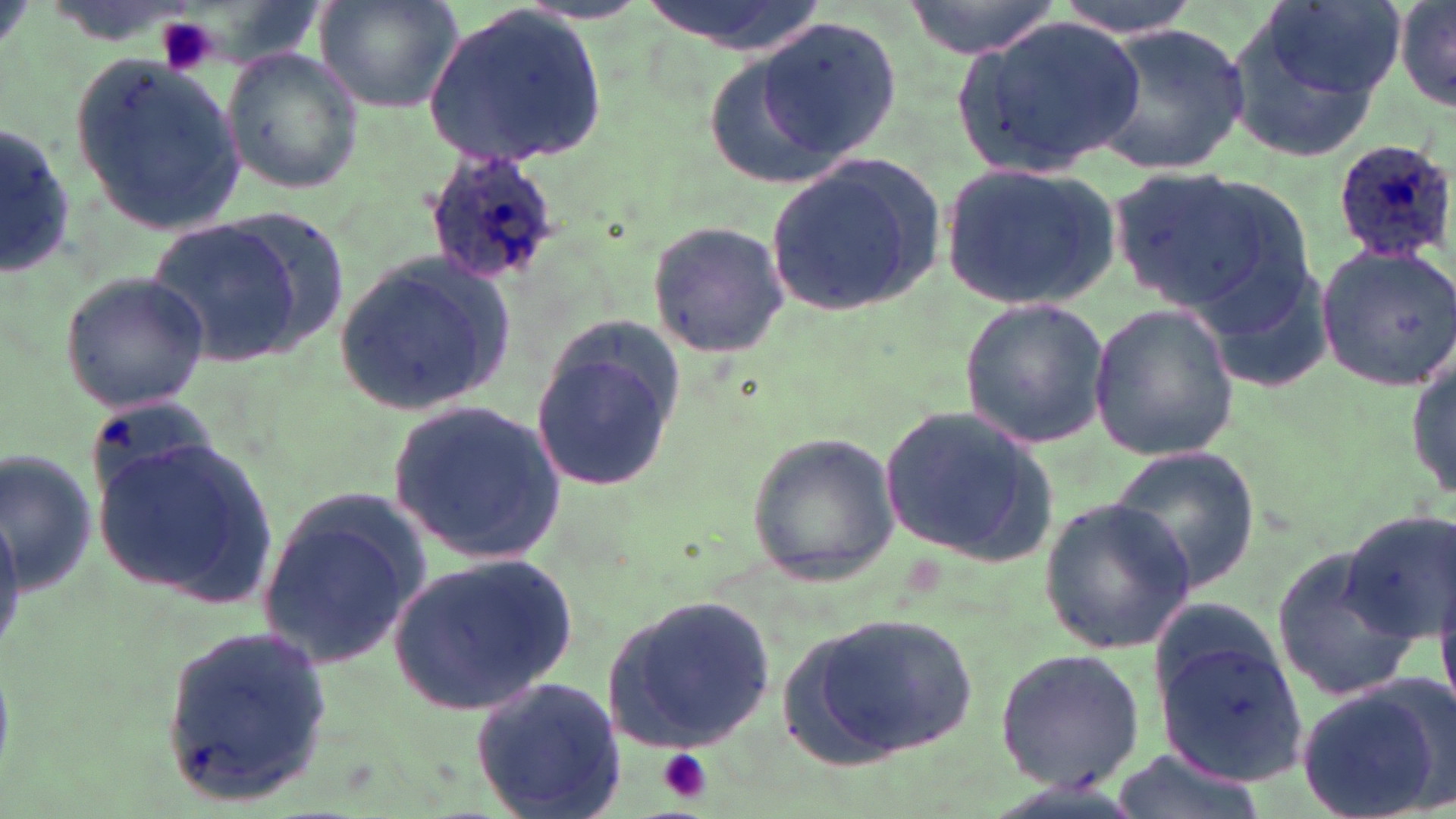
Summary:
  - Coordinate format: approximate bounding boxes as [x1, y1, x2, y2] in pixels
  - Uninfected red blood cell locations: [315, 0, 464, 115], [636, 0, 825, 55], [899, 0, 1070, 60], [1049, 0, 1201, 37], [1224, 0, 1404, 159], [1393, 0, 1455, 113], [424, 3, 605, 168], [954, 14, 1144, 180], [750, 16, 901, 169], [1087, 20, 1252, 177], [223, 47, 366, 196], [70, 50, 245, 235], [0, 127, 77, 278], [765, 152, 947, 319], [936, 161, 1121, 311], [1107, 163, 1311, 325], [149, 216, 306, 366], [644, 218, 792, 361], [1315, 242, 1456, 394], [333, 251, 518, 417], [58, 272, 210, 414], [957, 296, 1110, 450], [1086, 302, 1241, 462], [528, 318, 687, 496], [1408, 347, 1454, 504], [386, 397, 566, 566], [875, 400, 1059, 571], [93, 431, 280, 608], [743, 432, 899, 585], [1105, 447, 1261, 595], [3, 450, 99, 600], [257, 494, 431, 675], [1038, 497, 1200, 654], [1340, 510, 1455, 645], [1269, 544, 1422, 704], [385, 550, 577, 718], [597, 593, 778, 755], [792, 611, 982, 763], [1152, 622, 1307, 786], [158, 624, 334, 805], [992, 647, 1148, 795], [469, 673, 628, 819], [1295, 678, 1451, 819], [1110, 748, 1264, 819]
  - Platelet locations: [155, 18, 217, 77], [656, 750, 713, 804]
  - Plasmodium ovale-infected red blood cell locations: [1328, 138, 1455, 266], [421, 147, 559, 288]
  - Slide-level diagnosis: Plasmodium ovale
  - Magnification: 1000x
  - Stain: May-Grünwald-Giemsa
  - Image size: 1456×819 pixels
  - Preparation: thin blood film
  - Field of view: single
  - Modality: light microscopy